Assess this cell for malaria.
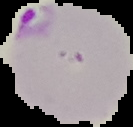
Parasitized.

Cell region segmented out of the field of view; the surrounding area is masked to black. Image is 133×127 pixels. From a thin blood smear.